Give the position of every malaria parasite.
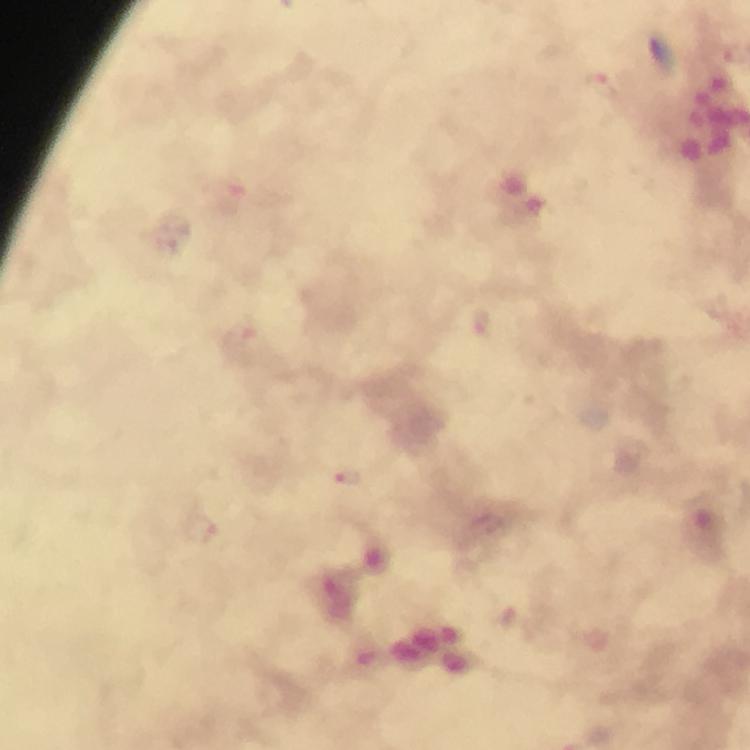

Approximate centers as {x, y} in pixels.
Malaria parasites: {601, 88}, {481, 323}, {346, 478}, {202, 528}.

From a diagnostic examination for malaria. Thick blood smear. Smartphone photograph taken through a microscope. Giemsa stain. Immersion oil was used. Cropped region of a single field of view. At 100x magnification. Image is 750×750 pixels.